Comment on the morphology of the red blood cells.
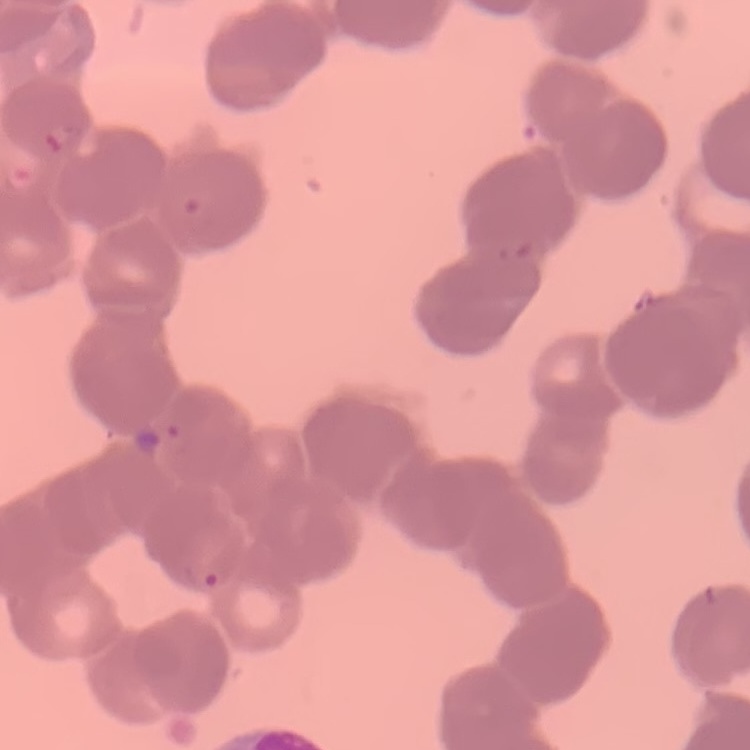
Rouleaux formation.

Field's or Giemsa stain. Thin blood smear. One tile cut from a larger photomicrograph.